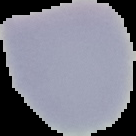

Summary:
  - Malaria status: uninfected
  - Image type: segmented cell region with the area outside set to black
  - Preparation: thin blood film
  - Image size: 136×136 pixels